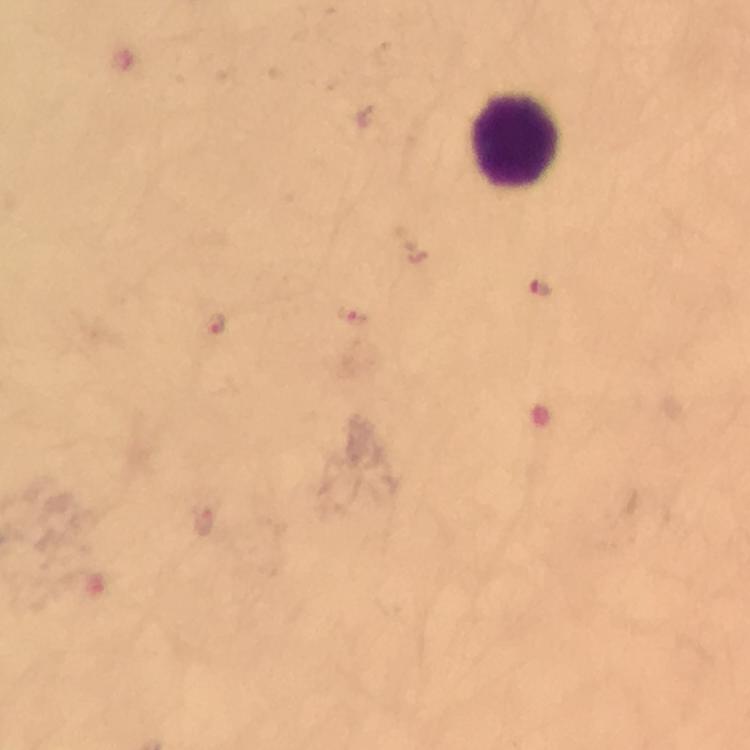

Approximate centers as [x, y] in pixels.
Summary:
  - Leukocyte locations: [514, 141]
  - Plasmodium parasite locations: [541, 289], [351, 318], [217, 325], [203, 520]
  - Magnification: 100x
  - Preparation: thick smear
  - Cropped from: one field of view
  - Capture: smartphone mounted on the microscope
  - Stain: Giemsa
  - Context: from a malaria diagnostic workup
  - Image size: 750×750 pixels
  - Immersion oil: used